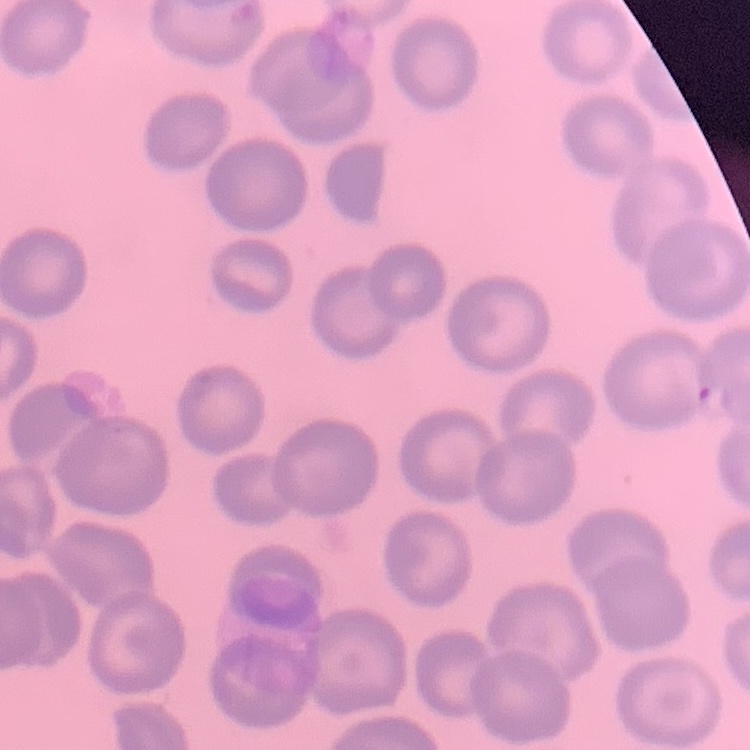
Summary:
  - Erythrocyte morphology: no rouleaux formation
  - Image type: one tile cut from a larger photomicrograph
  - Preparation: thin blood film
  - Stain: Field's or Giemsa